Identify the blood parasite species.
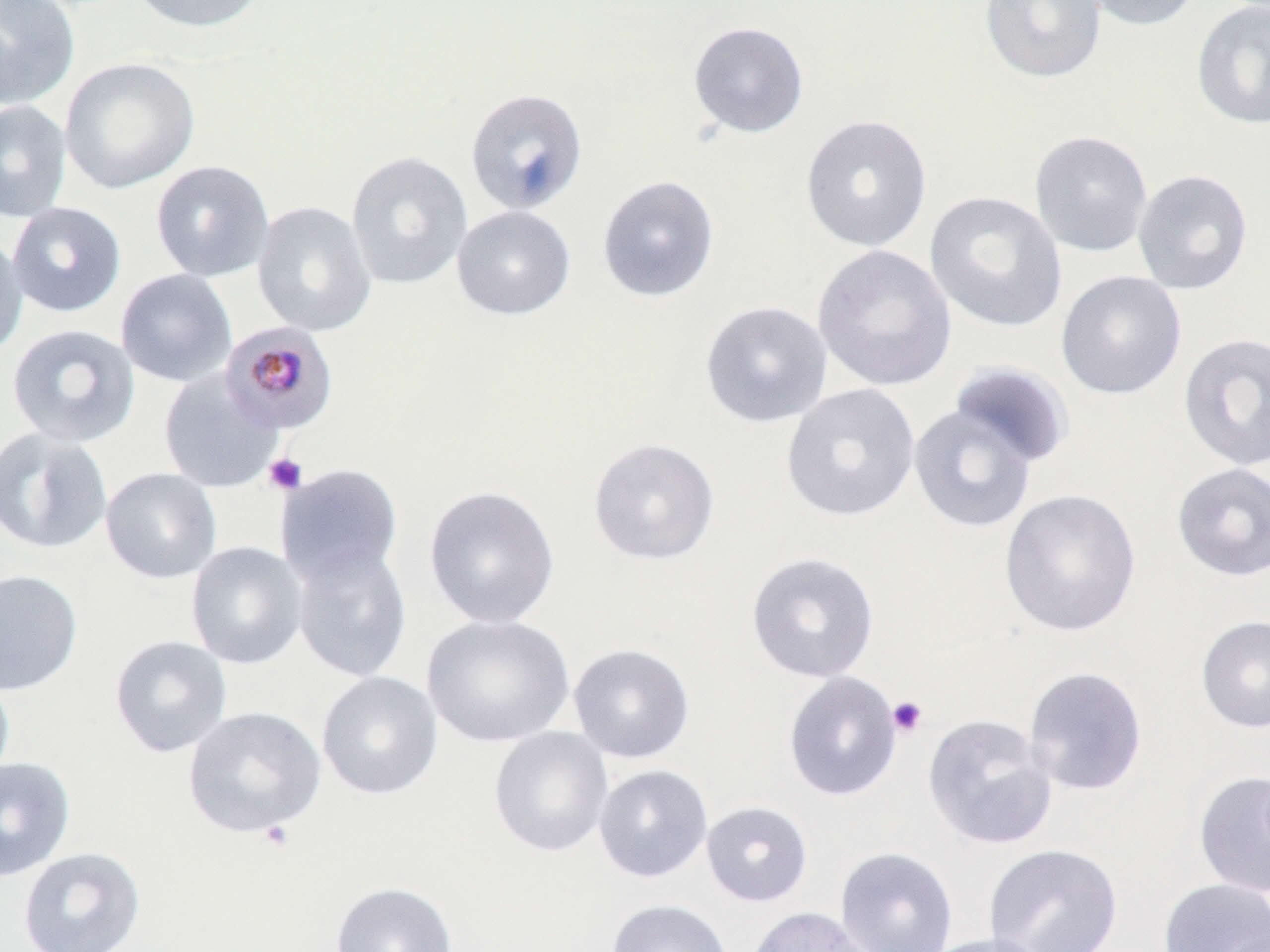

Plasmodium malariae.

image size = 1270×952 pixels
platelet locations = approximate bounding boxes as (x1,y1)-(x2,y2) corner pairs in pixels: (263,453)-(308,495), (887,696)-(928,738), (258,820)-(296,852)
stain = May-Grünwald-Giemsa
preparation = thin blood film
uninfected red blood cell locations = approximate bounding boxes as (x1,y1)-(x2,y2) corner pairs in pixels: (0,0)-(81,110), (124,0)-(269,34), (980,0)-(1107,84), (1075,0)-(1203,32), (1191,1)-(1270,130), (687,21)-(809,138), (59,57)-(200,194), (465,88)-(588,216), (0,100)-(72,223), (800,114)-(933,253), (1028,130)-(1154,258), (346,150)-(474,289), (150,160)-(275,282), (1132,169)-(1254,295), (596,174)-(720,303), (924,191)-(1067,333), (251,201)-(377,337), (6,202)-(126,317), (452,205)-(576,321), (0,230)-(28,360), (812,244)-(957,393), (115,268)-(237,388), (1056,270)-(1187,400), (699,300)-(833,428), (6,323)-(141,448), (1178,331)-(1270,471), (947,361)-(1074,471), (158,371)-(284,494), (781,384)-(921,522), (909,404)-(1038,534), (0,426)-(114,554), (587,436)-(721,565), (275,462)-(404,588), (1171,462)-(1270,581), (100,467)-(222,584), (423,485)-(561,630), (999,488)-(1141,638), (186,541)-(309,669), (291,543)-(412,682), (745,551)-(880,683), (0,569)-(84,696), (421,613)-(575,748), (1196,615)-(1270,733), (108,634)-(232,758), (567,642)-(695,763), (1023,666)-(1148,796), (316,671)-(443,800), (782,671)-(903,802), (0,672)-(15,790), (182,706)-(327,839), (922,713)-(1058,850), (488,727)-(614,857), (0,755)-(76,883), (593,764)-(713,883), (1193,770)-(1270,898), (700,800)-(813,907), (983,843)-(1123,952), (18,846)-(147,952), (835,847)-(958,952), (1157,877)-(1270,951), (330,880)-(459,952), (606,898)-(735,952), (747,906)-(877,952), (921,933)-(1055,952)
modality = light microscopy
Plasmodium malariae-infected red blood cell locations = approximate bounding boxes as (x1,y1)-(x2,y2) corner pairs in pixels: (219,321)-(339,435)
field of view = one of a larger specimen
magnification = 1000x